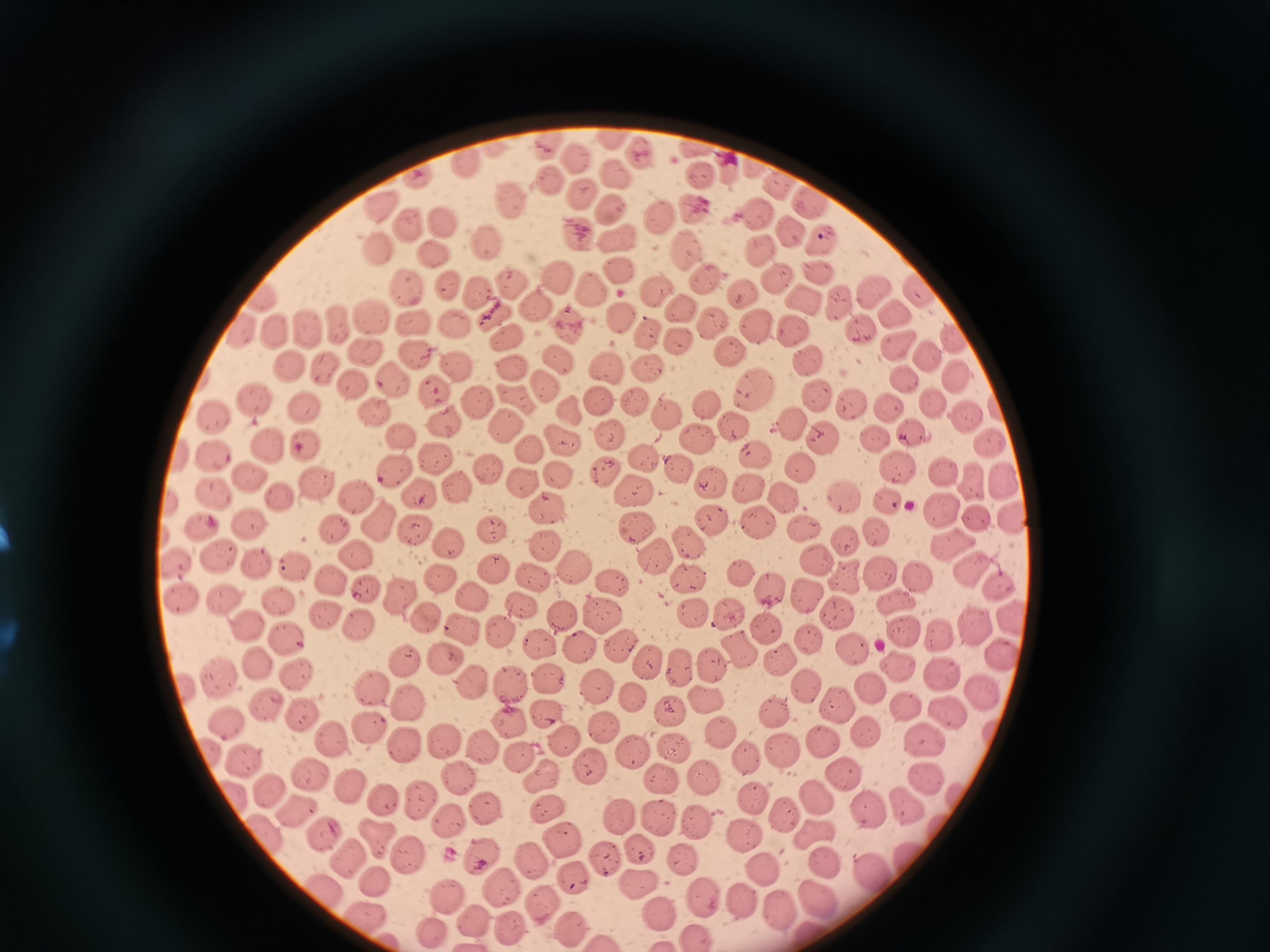
Approximate object centers, in pixels from the top-left corner.
Summary:
  - Cell locations: (x=612, y=138), (x=546, y=144), (x=639, y=149), (x=692, y=149), (x=572, y=157), (x=469, y=167), (x=728, y=168), (x=756, y=169), (x=618, y=175), (x=418, y=176), (x=700, y=177), (x=548, y=179), (x=784, y=188), (x=580, y=192), (x=510, y=198), (x=810, y=204), (x=383, y=206), (x=610, y=206), (x=692, y=208), (x=759, y=215), (x=661, y=218), (x=443, y=221), (x=410, y=223), (x=791, y=228), (x=577, y=229), (x=619, y=239), (x=824, y=242), (x=491, y=243), (x=374, y=246), (x=685, y=248), (x=762, y=253), (x=436, y=255), (x=618, y=269), (x=816, y=273), (x=558, y=275), (x=702, y=279), (x=779, y=280), (x=447, y=281), (x=511, y=283), (x=409, y=286), (x=594, y=287), (x=658, y=288), (x=878, y=291), (x=918, y=292), (x=477, y=293), (x=741, y=293), (x=260, y=298), (x=811, y=302), (x=843, y=303), (x=533, y=304), (x=677, y=309), (x=896, y=312), (x=496, y=314), (x=619, y=314), (x=373, y=316), (x=415, y=321), (x=711, y=321), (x=457, y=324), (x=340, y=325), (x=570, y=326), (x=791, y=326), (x=862, y=326), (x=308, y=327), (x=239, y=330), (x=760, y=330), (x=646, y=331), (x=282, y=333), (x=950, y=335), (x=504, y=336), (x=675, y=339), (x=732, y=348), (x=365, y=350), (x=903, y=351), (x=415, y=354), (x=806, y=359), (x=936, y=359), (x=559, y=361), (x=458, y=366), (x=607, y=366), (x=654, y=367), (x=292, y=368), (x=324, y=369), (x=508, y=370), (x=393, y=377), (x=906, y=379), (x=960, y=379), (x=348, y=382), (x=544, y=384), (x=436, y=389), (x=755, y=390), (x=816, y=395), (x=597, y=397), (x=632, y=399), (x=477, y=400), (x=514, y=400), (x=257, y=402), (x=849, y=404), (x=933, y=405), (x=305, y=407), (x=707, y=407), (x=892, y=409), (x=569, y=411), (x=665, y=411), (x=377, y=414), (x=216, y=415), (x=963, y=417), (x=442, y=419), (x=505, y=423), (x=735, y=427), (x=792, y=427), (x=404, y=434), (x=608, y=435), (x=875, y=436), (x=914, y=436), (x=699, y=439), (x=562, y=440), (x=827, y=441), (x=987, y=441), (x=268, y=447), (x=305, y=447), (x=531, y=450), (x=753, y=454), (x=216, y=455), (x=437, y=458), (x=644, y=458), (x=900, y=467), (x=393, y=469), (x=489, y=469), (x=608, y=470), (x=798, y=472), (x=560, y=473), (x=678, y=473), (x=944, y=474), (x=974, y=474), (x=247, y=475), (x=518, y=479), (x=315, y=482), (x=456, y=483), (x=712, y=483), (x=636, y=487), (x=1004, y=487), (x=748, y=488), (x=421, y=493), (x=218, y=494), (x=846, y=495), (x=356, y=496), (x=280, y=497), (x=785, y=501), (x=889, y=503), (x=546, y=509), (x=941, y=513), (x=975, y=517), (x=1012, y=520), (x=203, y=522), (x=380, y=523), (x=714, y=523), (x=755, y=523), (x=252, y=524), (x=637, y=526), (x=334, y=527), (x=413, y=530), (x=802, y=530), (x=492, y=532), (x=881, y=535), (x=686, y=541), (x=449, y=544), (x=850, y=544), (x=546, y=545), (x=950, y=547), (x=217, y=551), (x=358, y=554), (x=660, y=557), (x=819, y=560), (x=262, y=562), (x=178, y=563), (x=297, y=565), (x=574, y=565), (x=970, y=567), (x=494, y=569), (x=744, y=571), (x=533, y=574), (x=444, y=576), (x=883, y=576), (x=331, y=577), (x=919, y=577), (x=614, y=581), (x=848, y=581), (x=688, y=583), (x=1001, y=585), (x=772, y=586), (x=365, y=587), (x=402, y=594), (x=475, y=595), (x=811, y=597), (x=181, y=600), (x=228, y=600), (x=281, y=600), (x=899, y=603), (x=522, y=605), (x=691, y=611), (x=602, y=612), (x=326, y=613), (x=728, y=614), (x=426, y=615), (x=561, y=617), (x=1010, y=617), (x=247, y=621), (x=978, y=622), (x=360, y=623), (x=765, y=625), (x=464, y=628), (x=499, y=630), (x=909, y=632), (x=286, y=635), (x=808, y=636), (x=942, y=640), (x=541, y=642), (x=618, y=645), (x=582, y=646), (x=738, y=648), (x=850, y=649), (x=1004, y=651), (x=446, y=655), (x=403, y=661), (x=646, y=661), (x=709, y=662), (x=895, y=665), (x=258, y=666), (x=679, y=667), (x=296, y=673), (x=940, y=674), (x=217, y=675), (x=546, y=678), (x=470, y=681), (x=371, y=684), (x=511, y=684), (x=188, y=686), (x=809, y=687), (x=596, y=688), (x=985, y=689), (x=876, y=691), (x=635, y=698), (x=704, y=698), (x=406, y=701), (x=265, y=704), (x=839, y=705), (x=910, y=706), (x=671, y=709), (x=775, y=711), (x=952, y=711), (x=547, y=713), (x=304, y=716), (x=227, y=719), (x=508, y=721), (x=367, y=725), (x=602, y=726), (x=723, y=732), (x=866, y=732), (x=564, y=738), (x=822, y=738), (x=332, y=739), (x=441, y=740), (x=929, y=741), (x=406, y=742), (x=672, y=746), (x=483, y=747), (x=782, y=752), (x=636, y=754), (x=212, y=755), (x=519, y=755), (x=245, y=758), (x=747, y=759), (x=591, y=765), (x=844, y=771), (x=308, y=772), (x=459, y=774), (x=703, y=776), (x=542, y=777), (x=926, y=777), (x=664, y=779), (x=353, y=783), (x=269, y=787), (x=755, y=795), (x=816, y=796), (x=236, y=798), (x=421, y=798), (x=386, y=800), (x=482, y=804), (x=908, y=805), (x=546, y=806), (x=298, y=810), (x=871, y=812), (x=782, y=813), (x=620, y=819), (x=696, y=819), (x=657, y=820), (x=451, y=821), (x=325, y=831), (x=266, y=832), (x=818, y=833), (x=743, y=835), (x=563, y=839), (x=377, y=840), (x=639, y=848), (x=408, y=855), (x=479, y=855), (x=528, y=857), (x=353, y=858), (x=604, y=858), (x=683, y=861), (x=822, y=864), (x=762, y=868), (x=873, y=874), (x=573, y=875), (x=378, y=880), (x=639, y=880), (x=499, y=886), (x=445, y=891), (x=323, y=892), (x=702, y=895), (x=743, y=896), (x=819, y=896), (x=544, y=901), (x=780, y=908), (x=657, y=911), (x=364, y=915), (x=475, y=919), (x=511, y=923), (x=568, y=925), (x=433, y=928)
  - Image size: 1270×952 pixels
  - Capture: smartphone through the microscope eyepiece
  - Preparation: thin blood film
  - Stain: Giemsa
  - Field of view: single